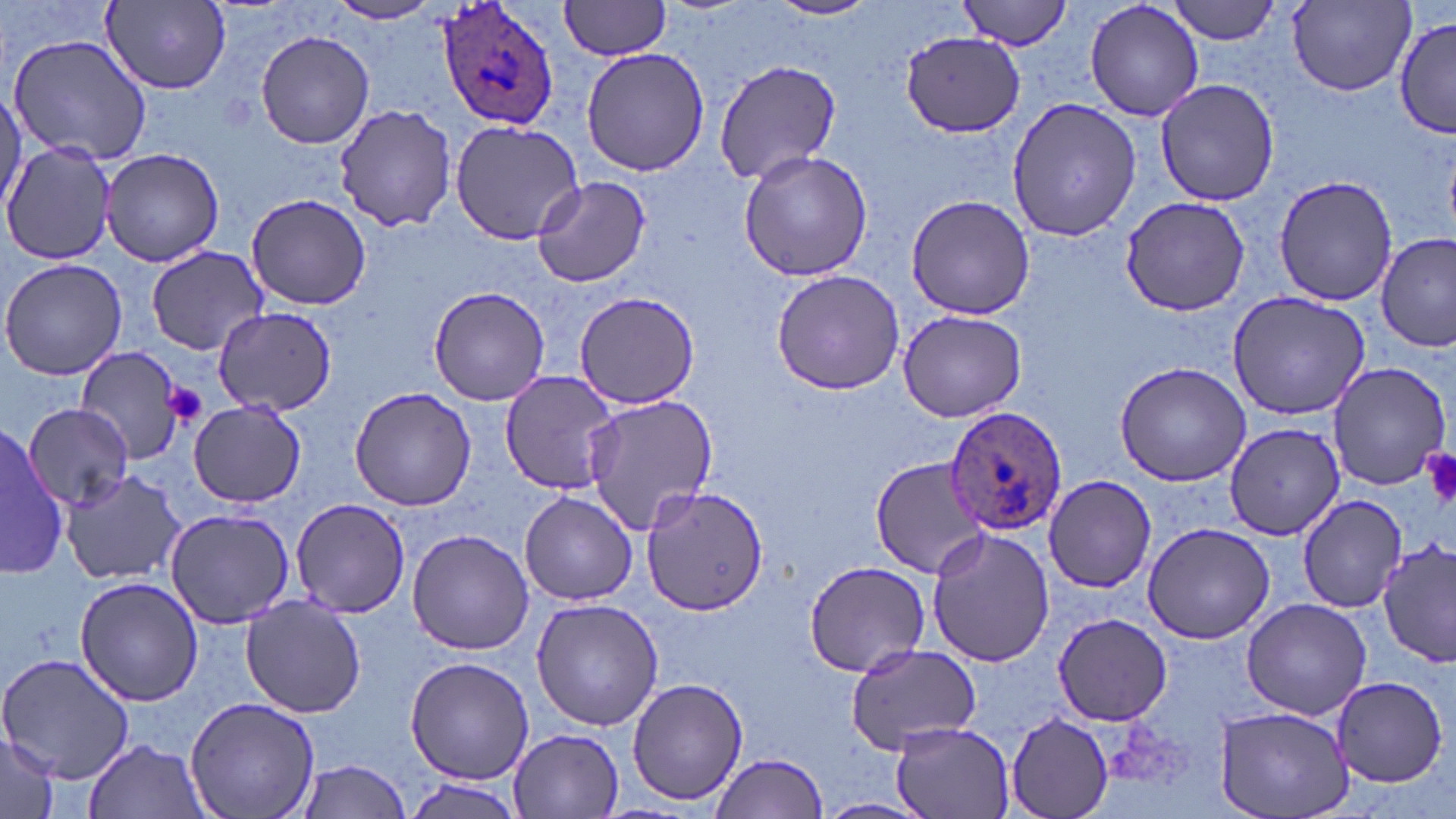
Approximate bounding boxes as (x1,y1)-(x2,y2) corner pairs in pixels. Plasmodium ovale-infected red blood cell locations: (435,0)-(561,131), (944,404)-(1066,536). Platelet locations: (161,382)-(208,427), (1420,446)-(1456,509). Uninfected red blood cell locations: (561,0)-(674,60), (767,0)-(882,21), (960,0)-(1072,50), (1084,0)-(1205,122), (1168,0)-(1284,44), (326,1)-(443,24), (103,2)-(232,91), (1290,2)-(1416,95), (1396,17)-(1452,138), (255,29)-(375,150), (900,31)-(1025,134), (5,33)-(154,169), (580,46)-(709,176), (714,58)-(841,185), (1154,78)-(1280,207), (0,88)-(24,213), (1008,96)-(1140,242), (333,103)-(457,231), (450,120)-(585,245), (2,142)-(119,264), (100,146)-(227,265), (737,149)-(877,282), (1275,175)-(1400,304), (532,176)-(651,288), (245,192)-(373,311), (905,193)-(1036,320), (1120,196)-(1253,317), (1377,233)-(1454,352), (145,245)-(267,354), (0,257)-(127,382), (770,270)-(908,394), (427,285)-(552,407), (574,290)-(699,410), (1225,292)-(1372,421), (211,305)-(336,416), (897,309)-(1025,422), (72,347)-(185,463), (1115,360)-(1251,488), (1326,360)-(1450,489), (500,370)-(624,495), (351,388)-(477,511), (580,392)-(719,535), (189,401)-(306,509), (22,403)-(135,511), (1224,424)-(1346,539), (1,425)-(67,576), (868,458)-(990,577), (61,468)-(188,587), (1044,473)-(1156,593), (641,484)-(770,614), (519,492)-(638,604), (1295,493)-(1408,612), (291,498)-(410,619), (164,508)-(297,629), (1141,520)-(1278,645), (925,526)-(1056,668), (407,529)-(534,655), (1378,539)-(1455,668), (804,559)-(929,677), (76,574)-(203,707), (239,594)-(368,718), (1239,597)-(1372,719), (531,598)-(663,731), (1053,614)-(1173,725), (846,645)-(981,752), (0,650)-(135,786), (405,657)-(533,783), (1330,675)-(1448,786), (626,677)-(748,807), (184,695)-(320,819), (1216,706)-(1353,819), (1006,713)-(1113,819), (889,721)-(1018,818), (509,728)-(625,817), (0,731)-(60,819), (83,737)-(212,819), (708,753)-(828,819), (294,759)-(413,819), (403,776)-(517,817), (817,796)-(934,819). Slide-level diagnosis: Plasmodium ovale. May-Grünwald-Giemsa stain. Optical microscopy. 1000x magnification. Thin blood smear. Single field of view. Image is 1456×819 pixels.